Locate and identify every blood parasite.
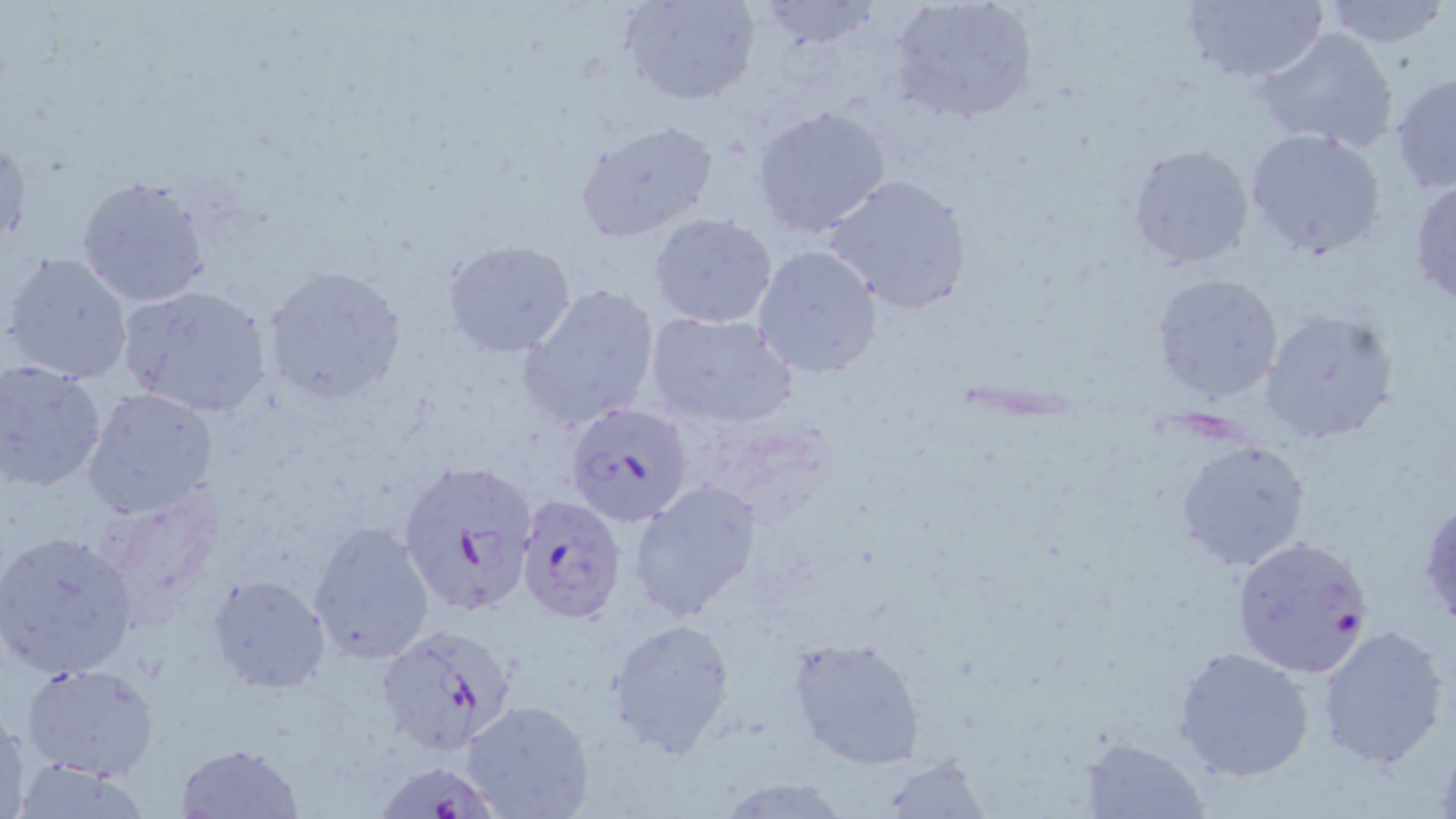
Approximate bounding boxes as (x1, y1, x2, y2) in pixels.
Plasmodium falciparum-infected red blood cells: (564, 400, 696, 526), (395, 457, 538, 620), (515, 494, 626, 624), (1230, 534, 1375, 677), (377, 624, 518, 755), (377, 759, 507, 819).
No Plasmodium ovale, Plasmodium malariae, Plasmodium vivax, Babesia divergens, or Trypanosoma brucei observed.

slide_level_diagnosis: Plasmodium falciparum
stain: May-Grünwald-Giemsa
modality: light microscopy
preparation: thin blood film
uninfected_red_blood_cell_locations: 'approximate bounding boxes as (x1, y1, x2, y2) in pixels: (618, 0, 761, 108), (753, 0, 887, 53), (887, 0, 1036, 125), (1180, 0, 1328, 84), (1318, 0, 1451, 49), (1254, 27, 1399, 154), (1389, 69, 1455, 194), (751, 103, 893, 239), (572, 119, 720, 244), (1243, 126, 1390, 261), (0, 133, 28, 251), (1126, 142, 1253, 270), (821, 173, 972, 315), (75, 175, 213, 309), (1409, 176, 1456, 304), (648, 214, 779, 329), (441, 237, 578, 358), (751, 244, 884, 379), (2, 251, 135, 387), (261, 266, 409, 406), (1152, 273, 1283, 402), (517, 281, 662, 431), (116, 282, 274, 417), (1259, 308, 1401, 445), (642, 309, 799, 430), (0, 359, 107, 492), (80, 386, 220, 522), (1174, 437, 1311, 572), (630, 481, 763, 621), (100, 488, 226, 616), (1418, 499, 1456, 631), (307, 522, 436, 665), (1, 528, 140, 679), (208, 574, 333, 695), (607, 618, 736, 755), (1315, 624, 1451, 769), (787, 636, 927, 768), (1172, 644, 1317, 783), (22, 663, 159, 782), (463, 700, 594, 819), (1, 706, 28, 818), (1079, 734, 1211, 817), (176, 743, 303, 819), (875, 756, 988, 818), (10, 760, 156, 817), (715, 775, 853, 817)'
image_size: 1456×819 pixels
field_of_view: one of a larger specimen
magnification: 1000x